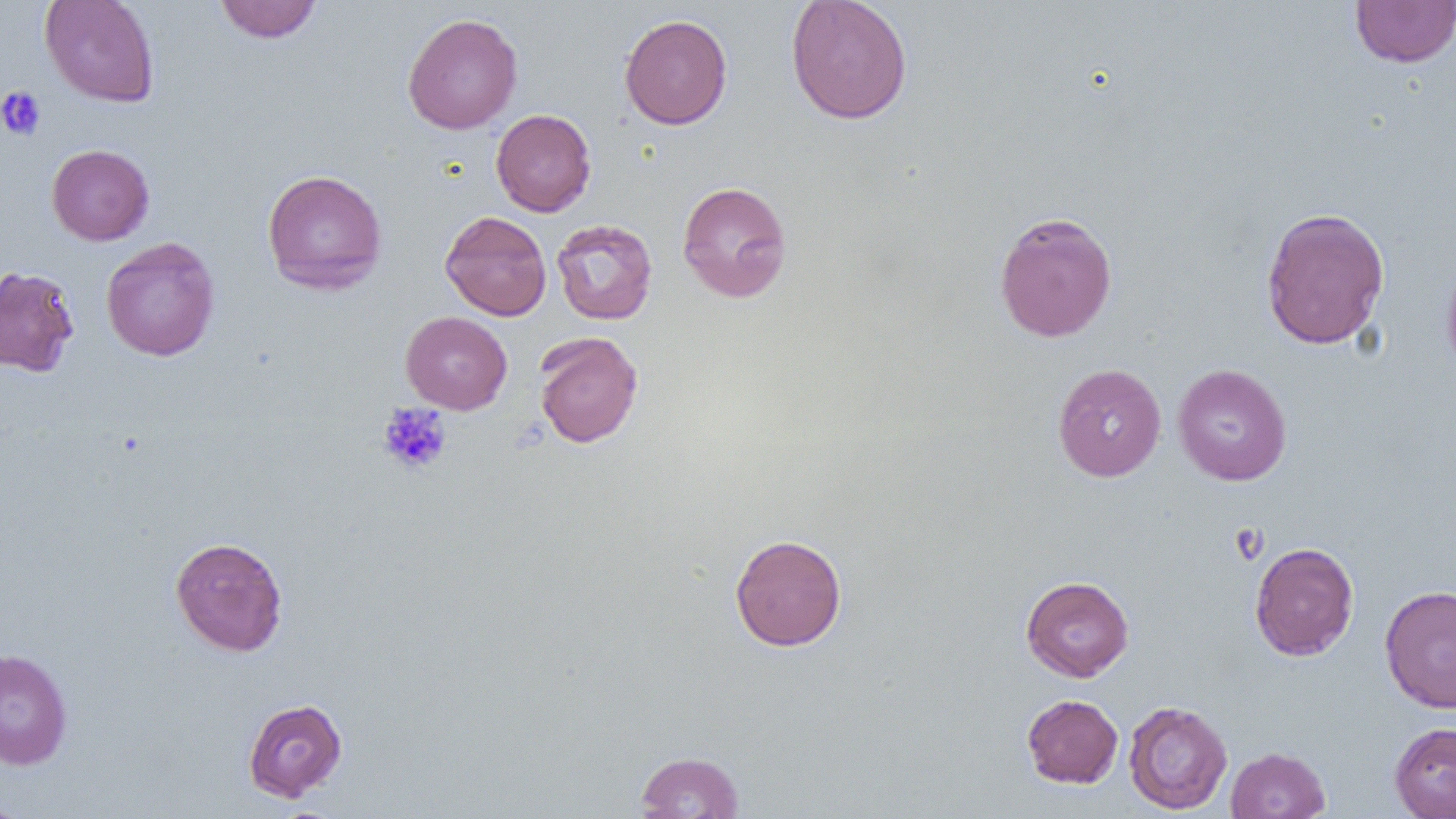
Approximate bounding boxes as (x1,y1)-(x2,y2) corner pairs in pixels. Platelet locations: (0,86)-(46,140), (377,402)-(452,475), (1230,523)-(1269,564). Uninfected red blood cell locations: (39,0)-(160,107), (214,0)-(322,43), (785,0)-(913,125), (1349,0)-(1456,68), (402,12)-(523,134), (619,14)-(733,129), (490,109)-(596,216), (46,144)-(154,245), (261,169)-(387,294), (677,181)-(793,303), (1260,206)-(1390,350), (440,211)-(552,321), (994,211)-(1118,342), (551,218)-(658,325), (101,237)-(220,362), (1440,252)-(1456,381), (0,265)-(80,376), (401,311)-(512,414), (534,331)-(643,448), (1052,363)-(1166,482), (1172,364)-(1292,486), (729,533)-(847,651), (170,536)-(288,656), (1249,541)-(1359,661), (1020,575)-(1134,682), (1379,584)-(1456,713), (0,648)-(73,770), (1022,694)-(1123,788), (1020,697)-(1232,793), (243,698)-(347,802), (1123,700)-(1232,815), (1389,721)-(1456,819), (1225,746)-(1331,818), (635,751)-(744,818), (0,793)-(28,819). Slide-level diagnosis: negative for blood parasites. Image is 1456×819 pixels. Thin blood smear. One field of a larger specimen. Light microscopy. Captured at 1000x magnification.